Assess the morphology of the erythrocytes.
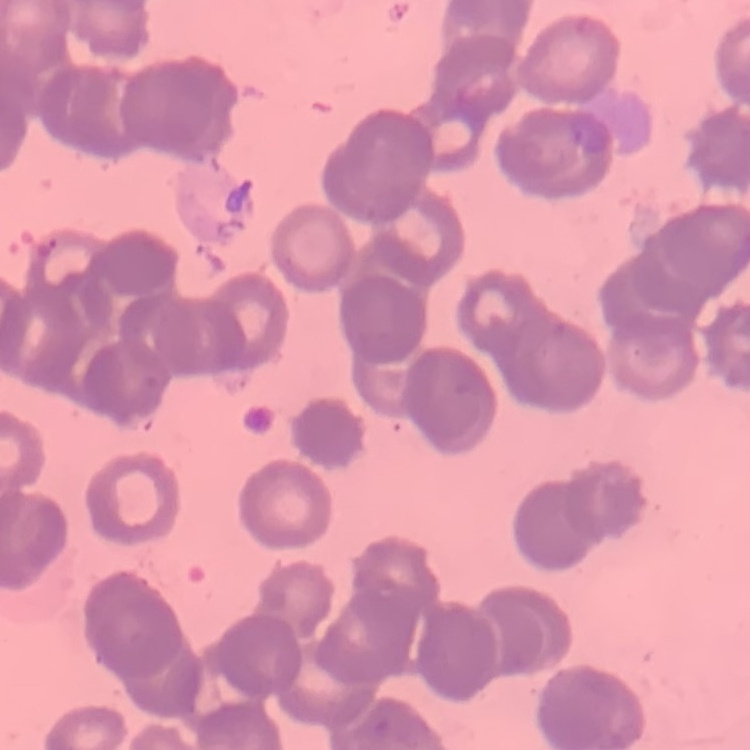

Rouleaux formation.

Thin blood smear. One tile cut from a larger photomicrograph. Field's or Giemsa stain.